Classify this cell by malaria status.
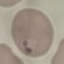
Parasitized.

Automatically extracted cell patch, resized to 64 × 64 pixels. Photographed with a smartphone camera at the microscope eyepiece. Thin blood smear. Giemsa stain.